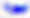

Toxoplasma gondii is shown. 400x magnification. Photomicrograph.